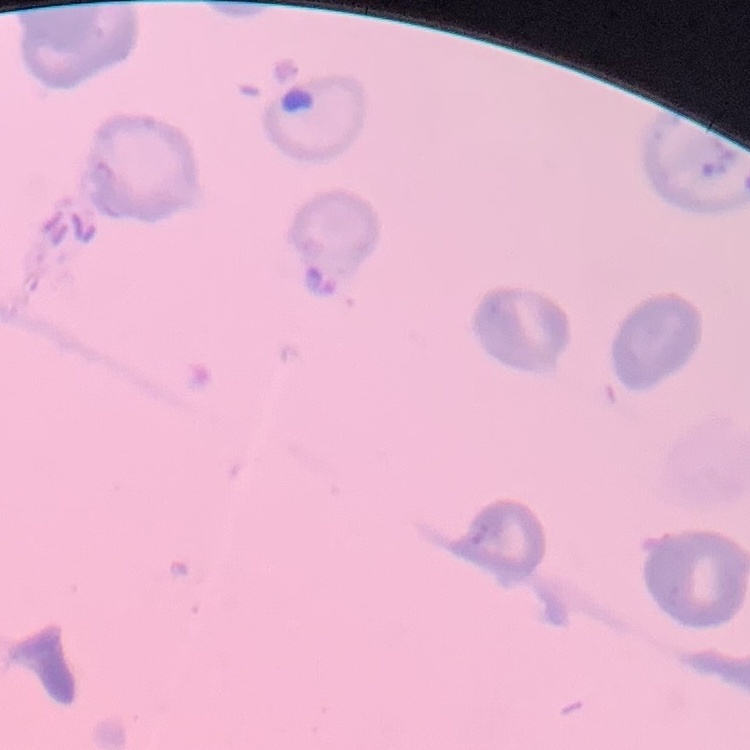
red blood cell morphology = no rouleaux formation
preparation = thin blood smear
stain = Field's or Giemsa
image type = one tile cut from a larger photomicrograph